Classify this cell by malaria status.
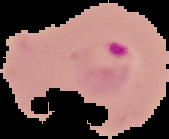
Parasitized.

Summary:
  - Image size: 169×139 pixels
  - Image type: segmented cell region with the area outside set to black
  - Preparation: thin blood film